Report the malaria status of this cell.
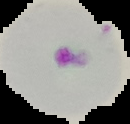
It is parasitized.

Cell region segmented out of the field of view; the surrounding area is masked to black. From a thin blood film. Image is 130×124 pixels.